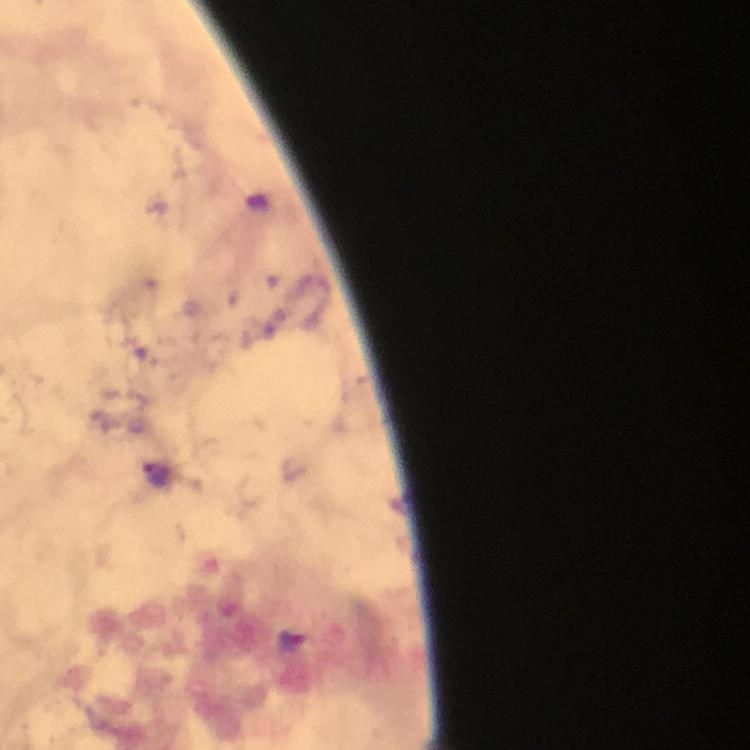
Approximate centers as [x, y] in pixels. Plasmodium parasite locations: [158, 476], [292, 639]. Photographed through the microscope with a smartphone camera. Immersion oil applied. From a diagnostic examination for malaria. Cropped region of a single field of view. At 100x magnification. Image is 750×750 pixels. Giemsa-stained preparation. Thick blood film.